Identify the cell.
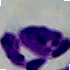

This is a leukocyte.

1000x magnification. Micrograph.